Give the location of every parasitized red blood cell.
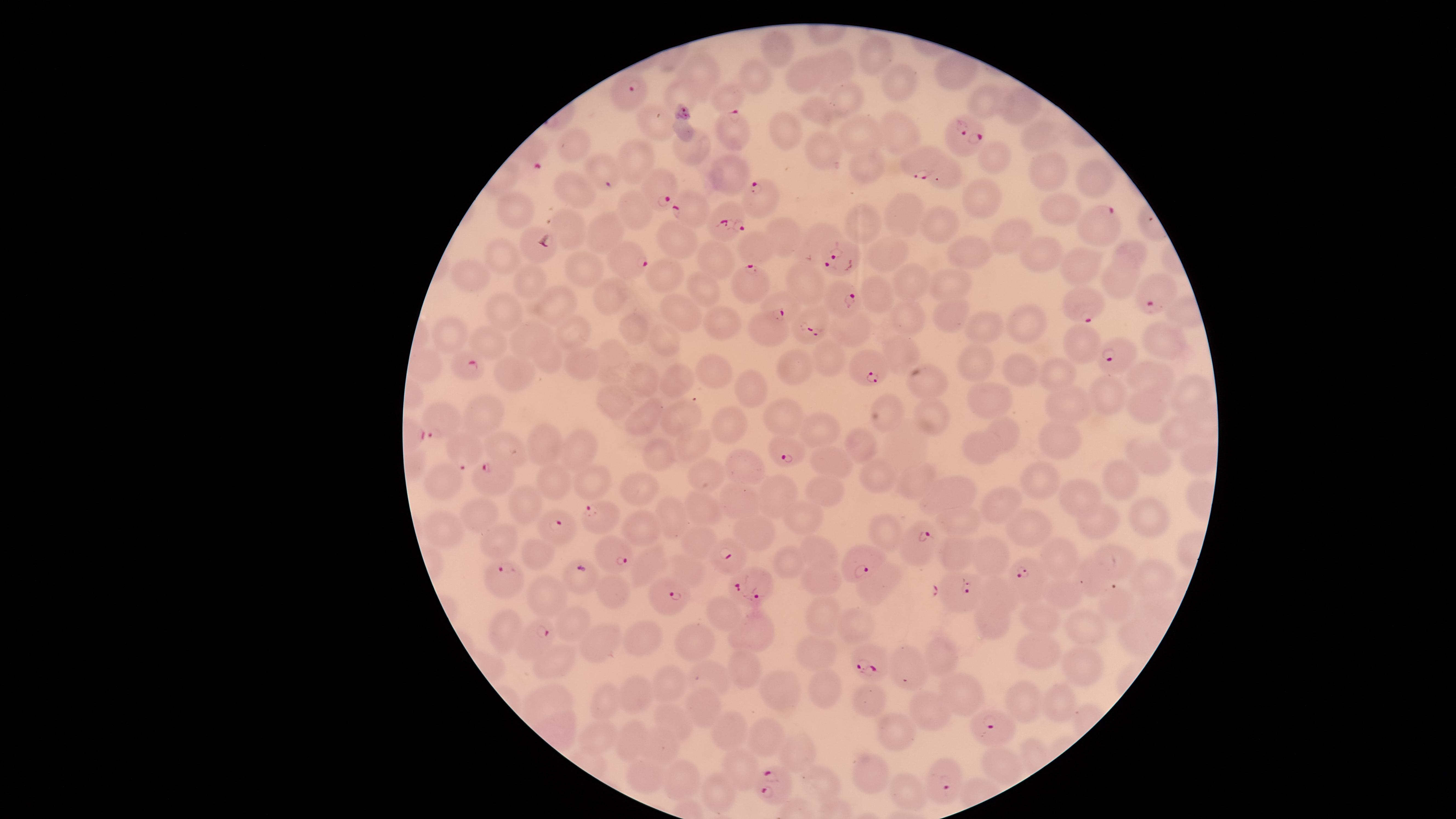

Approximate marker points as (x, y) in pixels.
Parasitized red blood cells: (625, 95), (732, 125), (966, 139), (925, 153), (660, 185), (760, 202), (688, 209), (726, 214), (1096, 223), (530, 243), (845, 257), (630, 259), (746, 284), (1146, 292), (836, 299), (1080, 306), (814, 324), (764, 328), (1112, 352), (468, 367), (871, 368), (436, 420), (788, 446), (463, 454), (488, 478), (605, 517), (560, 532), (916, 545), (609, 552), (725, 555), (863, 561), (1028, 572), (499, 577), (753, 581), (956, 590), (666, 597), (1116, 601), (535, 633), (871, 661), (991, 726), (944, 774), (774, 784).

field_of_view: single
preparation: thin smear of blood
species: Plasmodium falciparum
image_size: 1456×819 pixels
uninfected_red_blood_cells: 'approximate marker points as (x, y) in pixels: (870, 53), (839, 63), (699, 67), (801, 69), (757, 73), (891, 81), (688, 92), (727, 93), (843, 95), (978, 99), (1013, 101), (825, 113), (655, 119), (781, 125), (900, 127), (862, 133), (1036, 136), (577, 140), (694, 148), (826, 152), (998, 157), (638, 158), (865, 162), (1045, 164), (599, 169), (728, 172), (942, 172), (1088, 177), (571, 188), (990, 199), (511, 207), (630, 209), (1060, 211), (905, 214), (937, 219), (865, 223), (571, 229), (1004, 231), (604, 233), (818, 234), (783, 236), (681, 238), (970, 247), (757, 248), (888, 248), (502, 249), (1133, 250), (1030, 254), (718, 259), (1070, 264), (590, 272), (667, 273), (477, 274), (534, 277), (806, 279), (915, 281), (1122, 285), (704, 286), (957, 286), (878, 293), (609, 296), (551, 303), (684, 310), (504, 312), (908, 312), (952, 312), (716, 321), (1028, 326), (854, 327), (630, 328), (990, 329), (444, 331), (532, 335), (573, 335), (1157, 335), (1081, 339), (664, 340), (490, 342), (899, 349), (975, 356), (611, 358), (828, 359), (545, 360), (578, 362), (796, 365), (710, 366), (1016, 367), (426, 368), (1055, 371), (1150, 371), (513, 376), (642, 379), (676, 380), (931, 388), (1193, 388), (752, 390), (1104, 391), (986, 401), (617, 403), (1061, 406), (1150, 410), (649, 414), (680, 414), (488, 416), (781, 416), (934, 418), (889, 420), (823, 425), (723, 426), (1175, 427), (1009, 432), (1063, 436), (694, 442), (864, 443), (543, 445), (580, 447), (983, 447), (505, 449), (662, 450), (836, 456), (1148, 456), (744, 467), (1043, 477), (711, 478), (921, 478), (880, 479), (1121, 480), (443, 481), (551, 481), (592, 485), (638, 488), (957, 489), (783, 493), (829, 493), (1078, 494), (742, 503), (1002, 505), (527, 508), (695, 509), (670, 514), (483, 516), (797, 518), (1152, 518), (962, 520), (1098, 524), (639, 529), (445, 530), (882, 530), (1038, 530), (752, 535), (497, 542), (693, 543), (533, 553), (823, 553), (1057, 554), (957, 556), (993, 556), (1109, 558), (652, 563), (789, 564), (688, 572), (1148, 578), (877, 582), (820, 583), (1089, 584), (611, 592), (548, 596), (996, 597), (1065, 597), (822, 610), (723, 615), (988, 619), (1040, 619), (571, 621), (855, 622), (1085, 626), (755, 632), (508, 634), (641, 639), (691, 643), (596, 644), (1040, 647), (814, 653), (939, 653), (549, 660), (742, 667), (911, 667), (1078, 670), (711, 676), (666, 683), (829, 690), (958, 691), (636, 692), (779, 693), (550, 697), (875, 699), (1023, 705), (608, 706), (1061, 706), (703, 707), (926, 707), (677, 719), (902, 728), (732, 729), (602, 734), (770, 734), (638, 740), (661, 744), (801, 747), (1000, 763), (743, 767), (640, 773), (869, 776), (683, 781), (827, 784), (723, 789), (912, 791)'
capture: smartphone photograph through the microscope eyepiece
visible_region: circular
stain: Giemsa